Assess the morphology of the red blood cells.
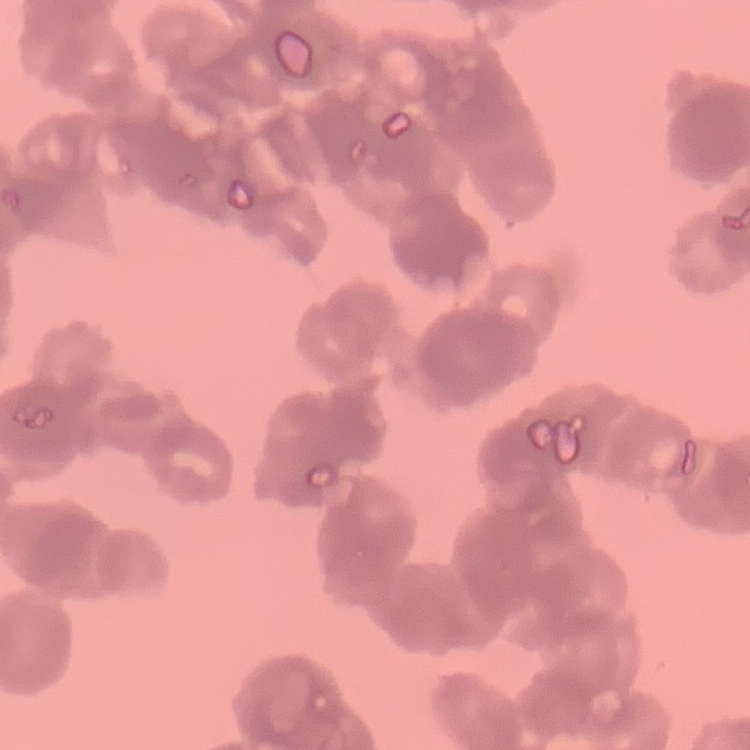

Rouleaux formation.

Thin blood film. Square crop of a larger photomicrograph. Field's or Giemsa stain.